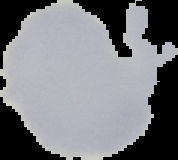
image_type: cell region segmented out of the field of view; surrounding area masked to black
image_size: 178×160 pixels
preparation: thin blood smear
result: no Plasmodium parasites detected